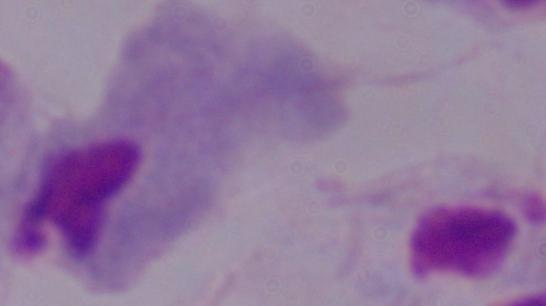 Captured at 1000x magnification. Photomicrograph. A trichomonad is shown.